Give the extent of all Plasmodium falciparum-infected red blood cells.
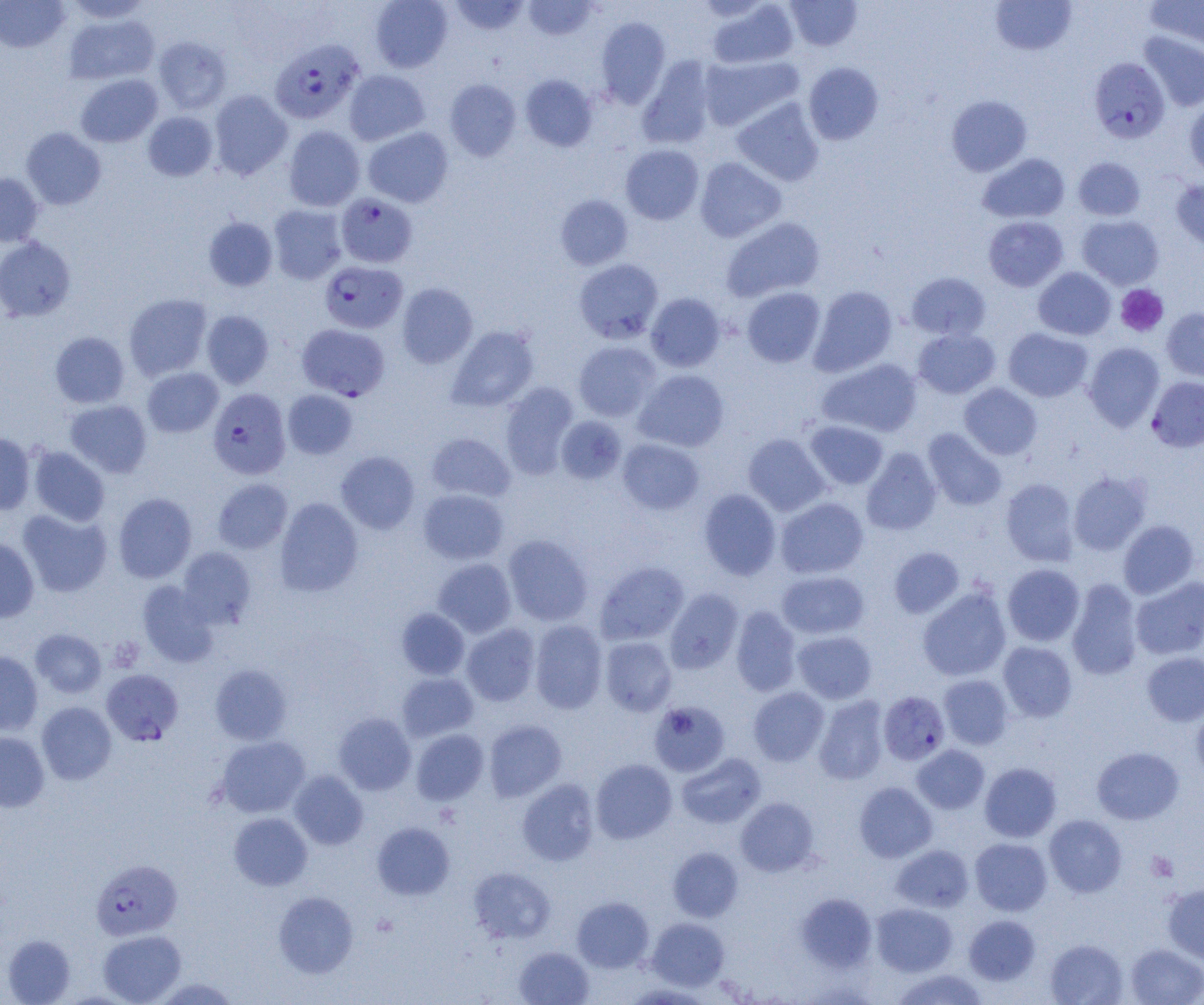

Approximate bounding boxes as (x1, y1, x2, y2) in pixels.
Plasmodium falciparum-infected red blood cells: (276, 39, 369, 124), (1088, 57, 1170, 143), (336, 194, 417, 268), (319, 261, 408, 333), (297, 323, 390, 400), (1147, 376, 1204, 452), (208, 388, 291, 479), (101, 668, 183, 745), (878, 691, 950, 765), (91, 858, 183, 940).

Uninfected red blood cell locations: (63, 0, 154, 23), (370, 0, 453, 72), (449, 0, 529, 35), (523, 0, 599, 40), (785, 0, 862, 51), (990, 0, 1077, 56), (1145, 0, 1204, 53), (0, 1, 69, 52), (707, 1, 799, 68), (64, 12, 160, 85), (595, 17, 670, 108), (1138, 31, 1204, 111), (153, 36, 232, 114), (699, 54, 802, 131), (636, 57, 717, 149), (803, 62, 884, 145), (344, 70, 430, 145), (76, 74, 162, 147), (520, 74, 598, 152), (445, 79, 521, 161), (209, 90, 292, 180), (946, 95, 1032, 176), (732, 98, 824, 186), (1184, 101, 1204, 178), (143, 111, 217, 181), (283, 126, 365, 211), (21, 127, 106, 210), (363, 127, 453, 207), (620, 144, 704, 224), (978, 153, 1070, 223), (694, 157, 787, 243), (1073, 157, 1146, 221), (0, 173, 44, 247), (1171, 178, 1204, 253), (555, 194, 633, 270), (268, 205, 348, 284), (1077, 215, 1164, 289), (203, 216, 278, 291), (721, 216, 825, 302), (983, 216, 1068, 292), (0, 236, 76, 322), (573, 258, 664, 344), (1033, 267, 1116, 340), (906, 272, 991, 341), (396, 283, 477, 368), (808, 285, 898, 376), (742, 287, 825, 368), (646, 293, 726, 372), (124, 294, 212, 381), (1161, 307, 1204, 383), (201, 310, 274, 389), (447, 325, 540, 413), (1003, 328, 1093, 402), (913, 329, 1000, 399), (50, 332, 130, 408), (574, 341, 661, 422), (1083, 342, 1164, 431), (817, 358, 922, 438), (142, 367, 223, 438), (634, 369, 729, 452), (500, 382, 579, 479), (959, 383, 1042, 460), (282, 390, 357, 459), (64, 400, 152, 478), (556, 415, 627, 484), (805, 420, 888, 489), (922, 428, 1007, 511), (0, 432, 35, 515), (425, 432, 515, 503), (743, 434, 830, 516), (617, 439, 703, 514), (28, 446, 110, 526), (861, 448, 941, 536), (336, 451, 420, 534), (1069, 471, 1151, 555), (212, 478, 292, 554), (1001, 478, 1079, 566), (418, 489, 509, 565), (698, 489, 781, 580), (113, 492, 197, 583), (275, 497, 363, 597), (775, 497, 869, 579), (18, 509, 112, 597), (1118, 520, 1199, 599), (503, 534, 593, 626), (0, 537, 39, 623), (177, 546, 257, 628), (889, 546, 964, 619), (433, 558, 516, 638), (595, 561, 689, 645), (1002, 564, 1085, 646), (777, 570, 869, 639), (1131, 577, 1204, 660), (1066, 579, 1143, 680), (137, 580, 218, 667), (917, 586, 1012, 681), (664, 588, 743, 674), (730, 606, 801, 696), (396, 608, 470, 679), (529, 620, 608, 714), (461, 623, 541, 706), (30, 628, 107, 698), (792, 631, 877, 704), (600, 637, 677, 716), (998, 641, 1078, 722), (0, 650, 43, 735), (1141, 652, 1204, 726), (210, 664, 292, 745), (397, 672, 479, 742), (938, 674, 1013, 749), (748, 686, 830, 766), (814, 696, 889, 784), (649, 700, 730, 776), (36, 701, 117, 784), (1191, 703, 1204, 781), (333, 712, 416, 795), (484, 720, 566, 802), (411, 729, 489, 805), (0, 731, 49, 812), (216, 736, 310, 818), (912, 744, 989, 814), (1092, 747, 1184, 824), (676, 753, 766, 828), (590, 759, 677, 843), (980, 762, 1061, 842), (289, 770, 368, 850), (517, 778, 599, 866), (854, 782, 937, 862), (736, 797, 818, 876), (229, 812, 312, 891), (1044, 814, 1127, 897), (372, 822, 455, 900), (970, 837, 1052, 916), (891, 844, 974, 912), (668, 847, 743, 922), (469, 867, 556, 944), (1162, 882, 1204, 964), (273, 891, 358, 978), (796, 892, 877, 972), (572, 896, 654, 972), (871, 903, 957, 976), (964, 915, 1040, 986), (647, 917, 729, 990), (97, 930, 186, 1004), (1, 934, 76, 1005), (1045, 938, 1128, 1004), (1125, 943, 1204, 1005), (514, 946, 594, 1005), (892, 969, 990, 1005), (621, 983, 715, 1004). Platelet locations: (1115, 285, 1169, 337), (1146, 851, 1178, 881). Slide-level diagnosis: Plasmodium falciparum. Thin blood film. Captured at 1000x magnification. Light microscopy. Single field of view. Image is 1204×1005 pixels.